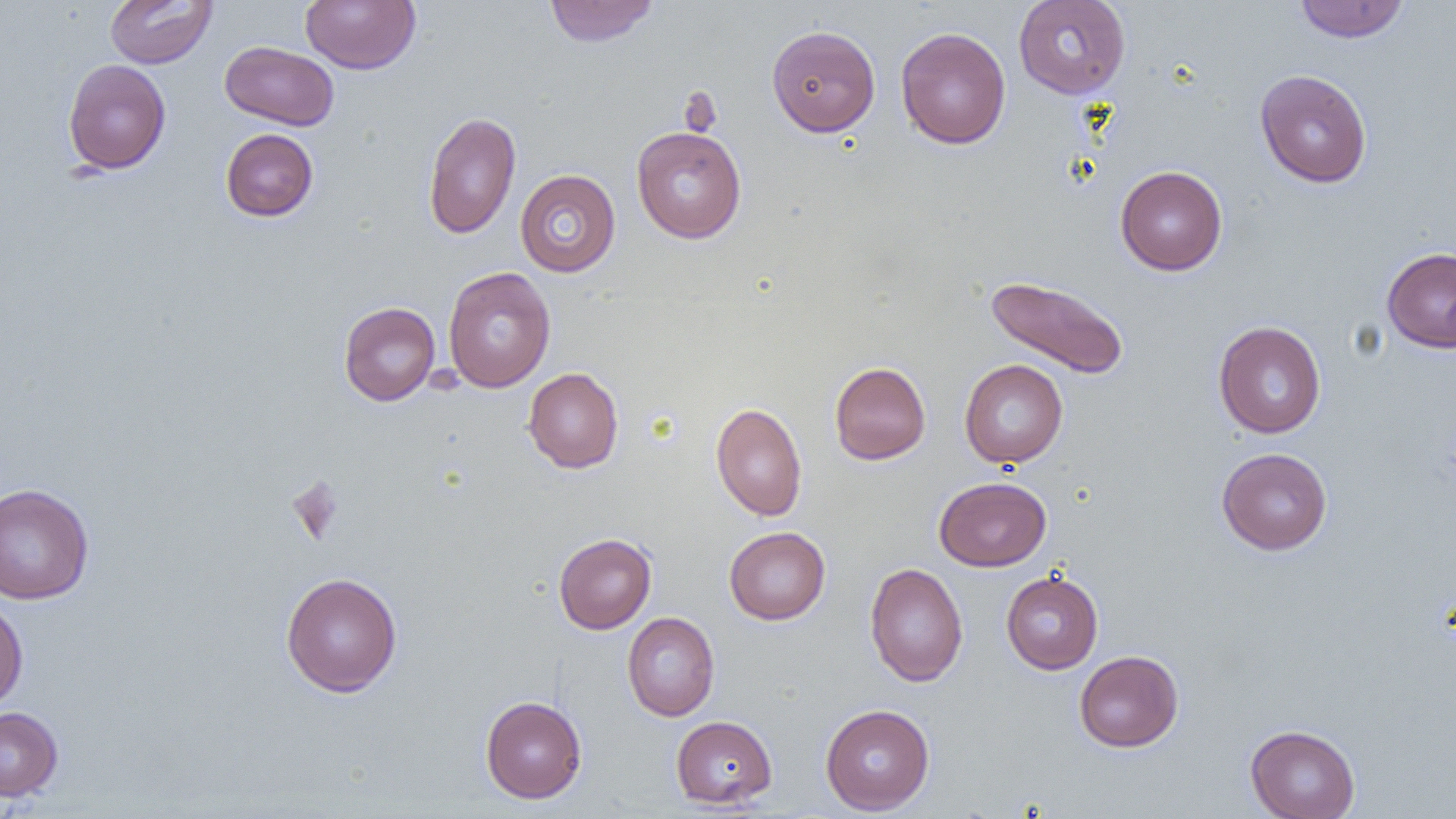

Approximate bounding boxes as [x1, y1, x2, y2] in pixels. Uninfected red blood cell locations: [105, 0, 217, 68], [544, 0, 659, 47], [1013, 0, 1130, 99], [301, 1, 420, 74], [1293, 1, 1409, 43], [766, 25, 880, 136], [896, 27, 1011, 150], [219, 40, 339, 131], [62, 59, 171, 174], [1255, 69, 1372, 188], [422, 111, 521, 239], [631, 126, 746, 243], [220, 128, 319, 222], [1115, 165, 1228, 275], [515, 169, 620, 277], [1381, 246, 1456, 353], [443, 267, 556, 392], [984, 274, 1131, 380], [338, 302, 440, 406], [1213, 320, 1326, 438], [959, 359, 1068, 468], [829, 361, 930, 464], [523, 367, 623, 473], [710, 402, 808, 521], [1216, 447, 1333, 554], [934, 476, 1051, 571], [0, 482, 94, 605], [724, 526, 830, 625], [553, 533, 656, 634], [864, 562, 968, 687], [280, 571, 402, 697], [1001, 571, 1103, 674], [0, 597, 28, 711], [622, 612, 719, 721], [1075, 650, 1183, 752], [480, 695, 587, 803], [820, 704, 935, 814], [0, 706, 63, 801], [671, 715, 777, 808], [1245, 724, 1360, 819]. Slide-level diagnosis: negative for blood parasites. Image is 1456×819 pixels. One field of a larger specimen. Optical microscopy. 1000x magnification. Thin blood film.